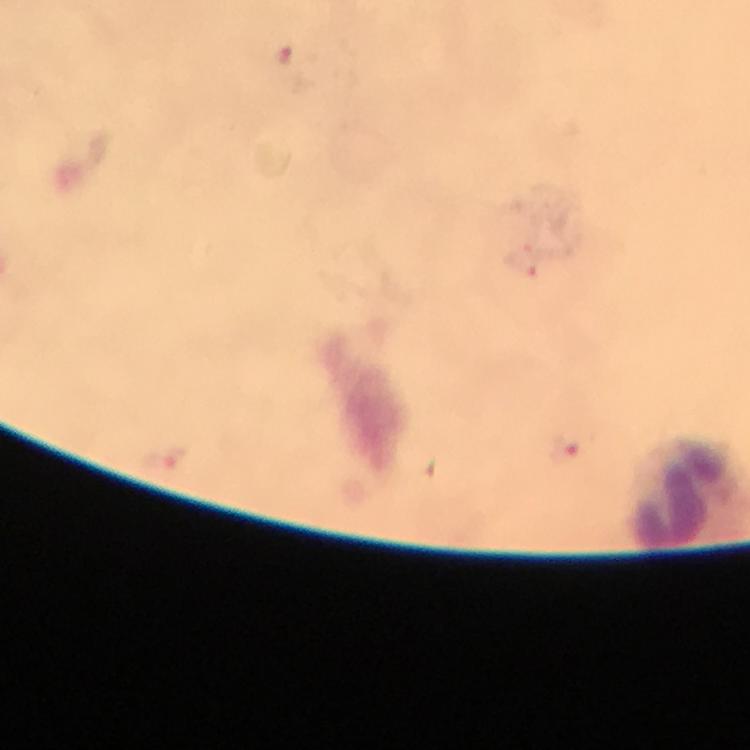
Approximate centers as (x, y) in pixels.
Summary:
  - Malaria parasite locations: (284, 54), (524, 262), (564, 449), (166, 458)
  - Capture: smartphone camera through the microscope
  - Image size: 750×750 pixels
  - Stain: Giemsa
  - Preparation: thick smear
  - Magnification: 100x
  - Cropped from: a single field of view
  - Immersion oil: applied
  - Context: from a malaria diagnostic workup